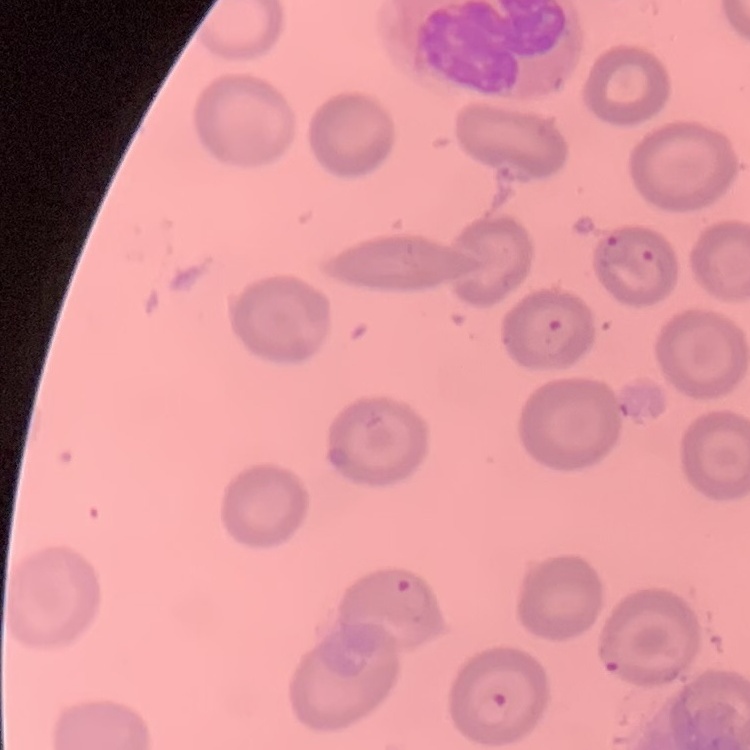

erythrocyte_morphology: no rouleaux formation
image_type: one tile cut from a larger photomicrograph
stain: Field's or Giemsa
preparation: thin blood film